Locate every Plasmodium parasite.
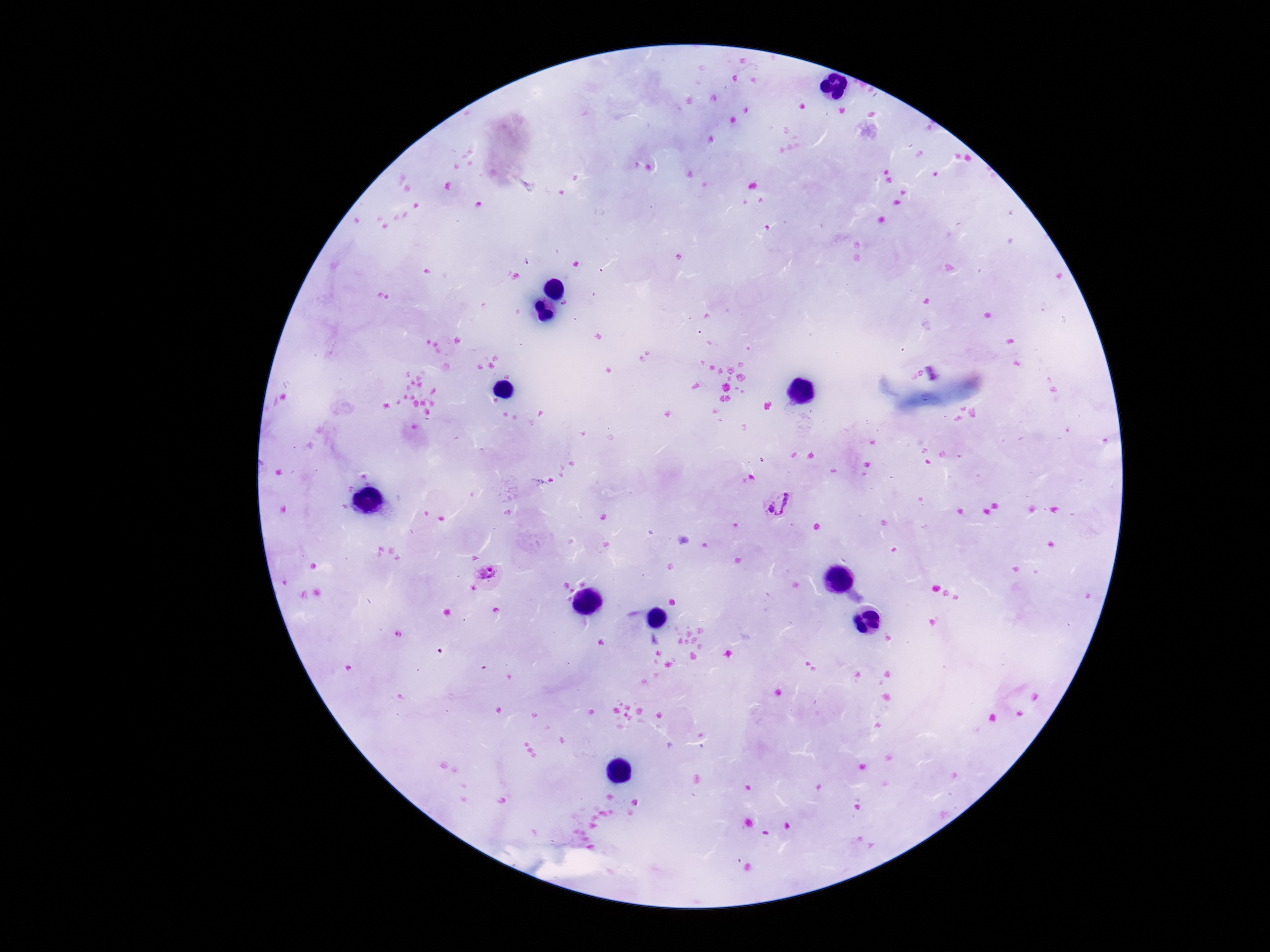

Approximate centers as [x, y] in pixels.
Plasmodium parasites: [778, 504], [487, 574].

Thick peripheral-blood smear. Photographed through the microscope eyepiece with a smartphone camera. One field from this slide. Patient malaria status: infected. Giemsa-stained preparation. 100x magnification. Image is 1270×952 pixels.